Evaluate for malaria.
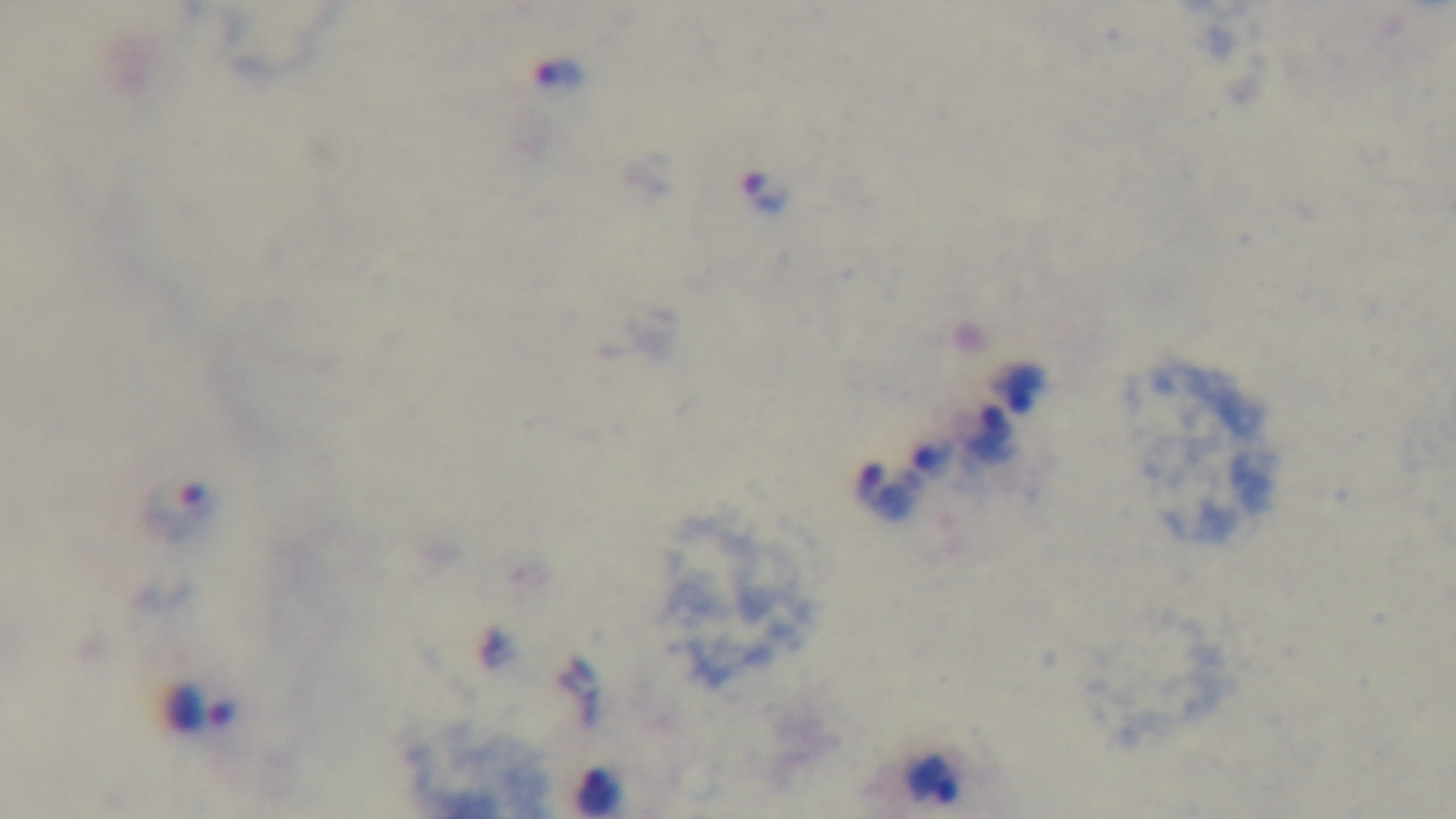
It is infected.

Summary:
  - Objective: 100x oil immersion
  - Preparation: thick blood film
  - Stain: Giemsa
  - Field of view: one from the slide
  - Capture: mounted 4K digital camera
  - Modality: light microscopy